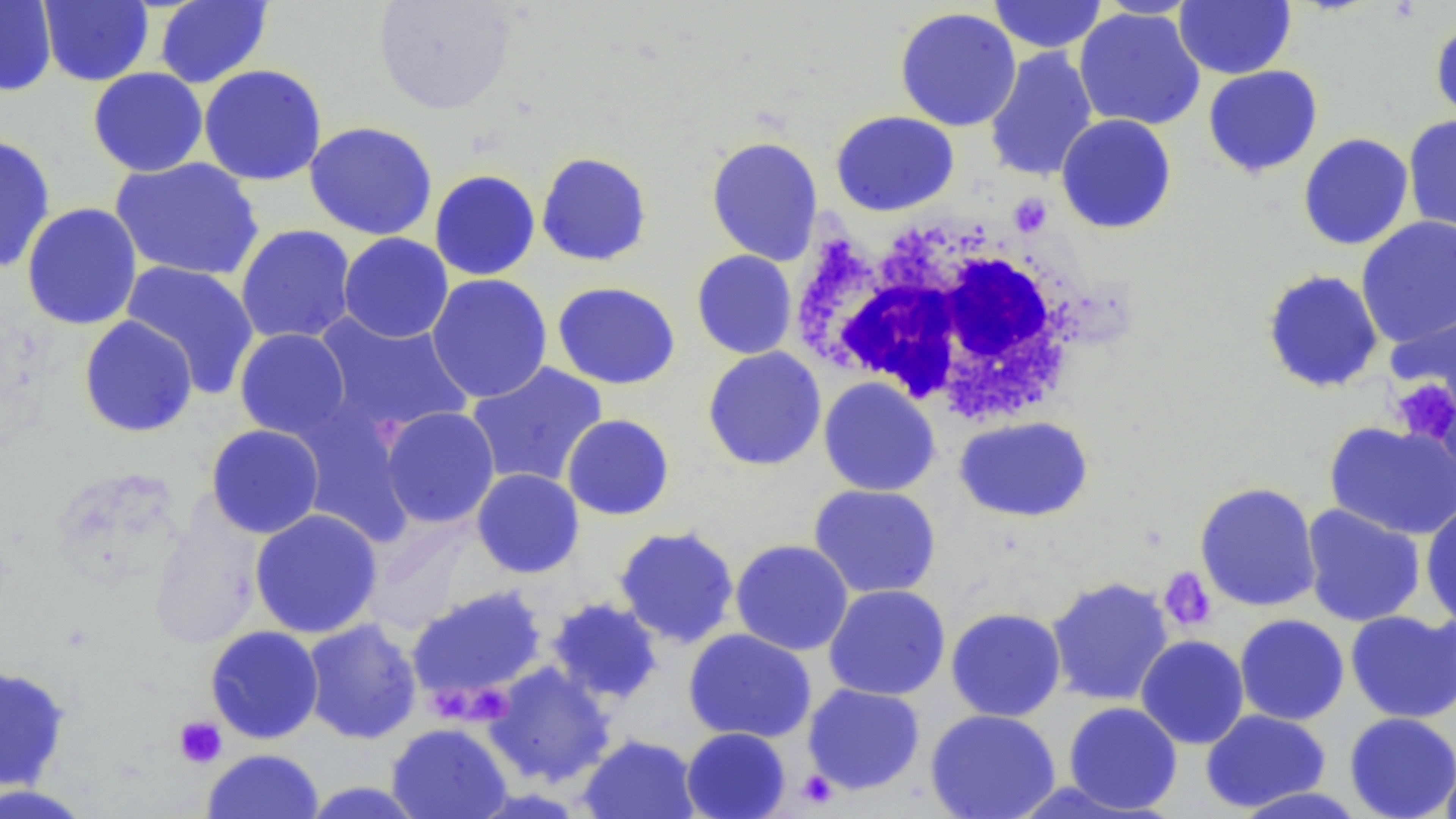 Approximate bounding boxes as (x1, y1, x2, y2) in pixels. Uninfected red blood cell locations: (0, 0, 57, 97), (373, 0, 519, 116), (987, 0, 1109, 54), (1089, 0, 1205, 19), (38, 1, 154, 87), (154, 1, 273, 88), (1174, 1, 1296, 79), (895, 6, 1022, 132), (1074, 6, 1206, 131), (1430, 16, 1456, 127), (983, 47, 1099, 183), (198, 64, 327, 186), (1202, 65, 1323, 177), (87, 67, 208, 177), (830, 110, 959, 216), (1055, 114, 1177, 234), (1402, 114, 1456, 238), (303, 121, 438, 240), (1298, 133, 1414, 250), (0, 134, 56, 273), (705, 136, 823, 266), (535, 151, 653, 266), (110, 157, 264, 281), (429, 169, 541, 281), (21, 202, 142, 330), (1355, 216, 1456, 347), (235, 225, 357, 345), (338, 233, 454, 343), (691, 250, 797, 360), (120, 260, 261, 398), (1261, 269, 1384, 393), (426, 274, 552, 403), (552, 281, 680, 390), (1386, 301, 1456, 422), (311, 312, 476, 440), (78, 315, 199, 438), (234, 328, 352, 440), (702, 347, 827, 471), (465, 362, 608, 490), (818, 377, 940, 496), (379, 406, 500, 528), (561, 414, 675, 520), (954, 416, 1093, 522), (1324, 420, 1456, 541), (205, 424, 325, 538), (471, 468, 584, 579), (1194, 482, 1321, 612), (808, 484, 941, 599), (1420, 500, 1456, 627), (1300, 504, 1426, 627), (148, 507, 265, 651), (249, 508, 383, 639), (613, 525, 740, 648), (730, 539, 854, 656), (1046, 577, 1174, 707), (406, 584, 548, 705), (823, 584, 950, 701), (546, 598, 663, 705), (945, 607, 1066, 722), (1345, 610, 1456, 723), (1234, 614, 1349, 726), (301, 618, 422, 745), (205, 626, 324, 744), (683, 629, 817, 743), (1135, 635, 1250, 749), (484, 662, 615, 787), (0, 664, 71, 791), (802, 683, 926, 795), (1063, 701, 1183, 814), (925, 709, 1061, 819), (1200, 709, 1331, 813), (1344, 712, 1456, 819), (386, 722, 512, 819), (680, 727, 792, 819), (578, 734, 701, 819), (202, 748, 323, 819), (1439, 755, 1456, 819), (298, 781, 430, 818), (0, 783, 97, 818), (1233, 785, 1368, 818). Platelet locations: (1390, 378, 1456, 448), (1159, 567, 1217, 632), (432, 680, 469, 719), (475, 688, 515, 725), (173, 715, 227, 768), (796, 770, 839, 808). White blood cell locations: (802, 212, 1094, 423). Slide-level diagnosis: no evidence of blood parasites. 1000x magnification. Image is 1456×819 pixels. May-Grünwald-Giemsa stain. Thin blood smear. Optical microscopy. One field of a larger specimen.